Classify this cell by malaria status.
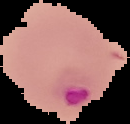

Parasitized.

From a thin blood film. The area outside the segmented cell region is set to black. Image is 130×124 pixels.